Outline each blood parasite and name the species.
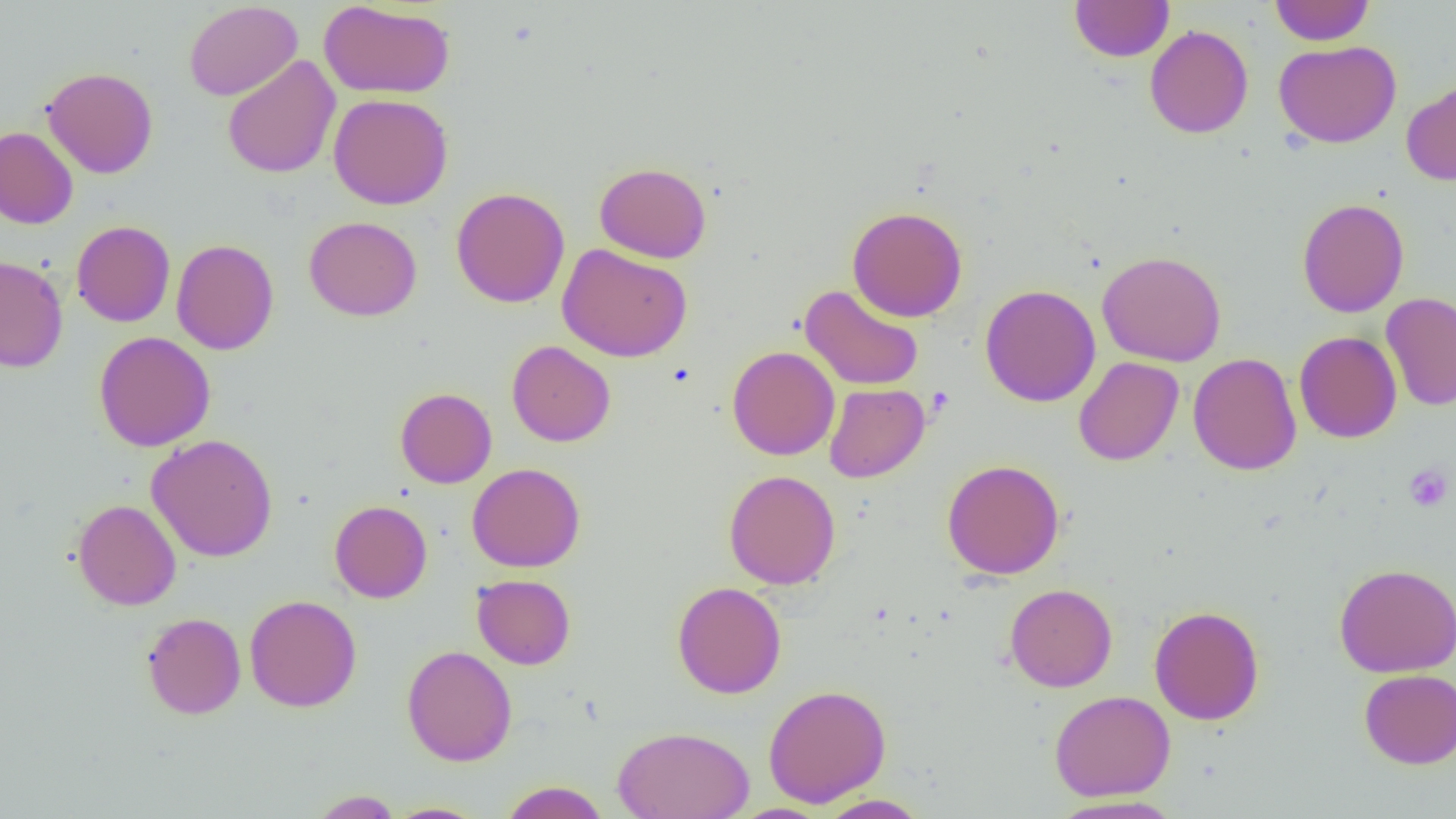

No blood parasites seen.

Summary:
  - Coordinate format: approximate bounding boxes as (x1,y1)-(x2,y2) corner pairs in pixels
  - Uninfected red blood cell locations: (318,0)-(455,99), (1070,0)-(1174,62), (1270,0)-(1374,45), (183,1)-(303,101), (1145,25)-(1253,138), (1274,40)-(1402,148), (222,55)-(340,179), (41,66)-(158,178), (1401,77)-(1456,186), (328,93)-(453,209), (0,126)-(78,229), (594,162)-(711,263), (451,187)-(570,308), (1297,198)-(1409,317), (847,205)-(967,322), (303,216)-(422,321), (71,220)-(175,327), (171,239)-(279,355), (557,243)-(692,362), (1097,250)-(1227,367), (0,255)-(68,372), (799,284)-(925,391), (980,284)-(1101,407), (1381,293)-(1456,411), (94,331)-(215,451), (1294,331)-(1402,443), (506,340)-(616,447), (727,345)-(839,460), (1188,353)-(1303,475), (1073,357)-(1184,466), (824,383)-(929,483), (395,387)-(497,488), (147,434)-(278,562), (941,459)-(1065,580), (467,462)-(585,572), (723,469)-(841,589), (72,499)-(181,610), (330,500)-(432,603), (1333,563)-(1456,678), (472,574)-(575,669), (672,581)-(786,699), (1004,583)-(1118,692), (244,594)-(362,713), (1149,605)-(1265,725), (142,612)-(246,719), (402,645)-(517,766), (1359,669)-(1456,769), (762,684)-(892,807), (1049,690)-(1176,801), (613,726)-(755,819), (499,780)-(610,819), (307,790)-(404,818), (815,794)-(932,818), (1046,795)-(1186,819), (382,802)-(491,818), (726,804)-(834,819)
  - Platelet locations: (1404,464)-(1453,513)
  - Slide-level diagnosis: no evidence of blood parasites
  - Magnification: 1000x
  - Field of view: one of a larger specimen
  - Preparation: thin blood film
  - Image size: 1456×819 pixels
  - Modality: optical microscopy